Locate and identify every blood parasite.
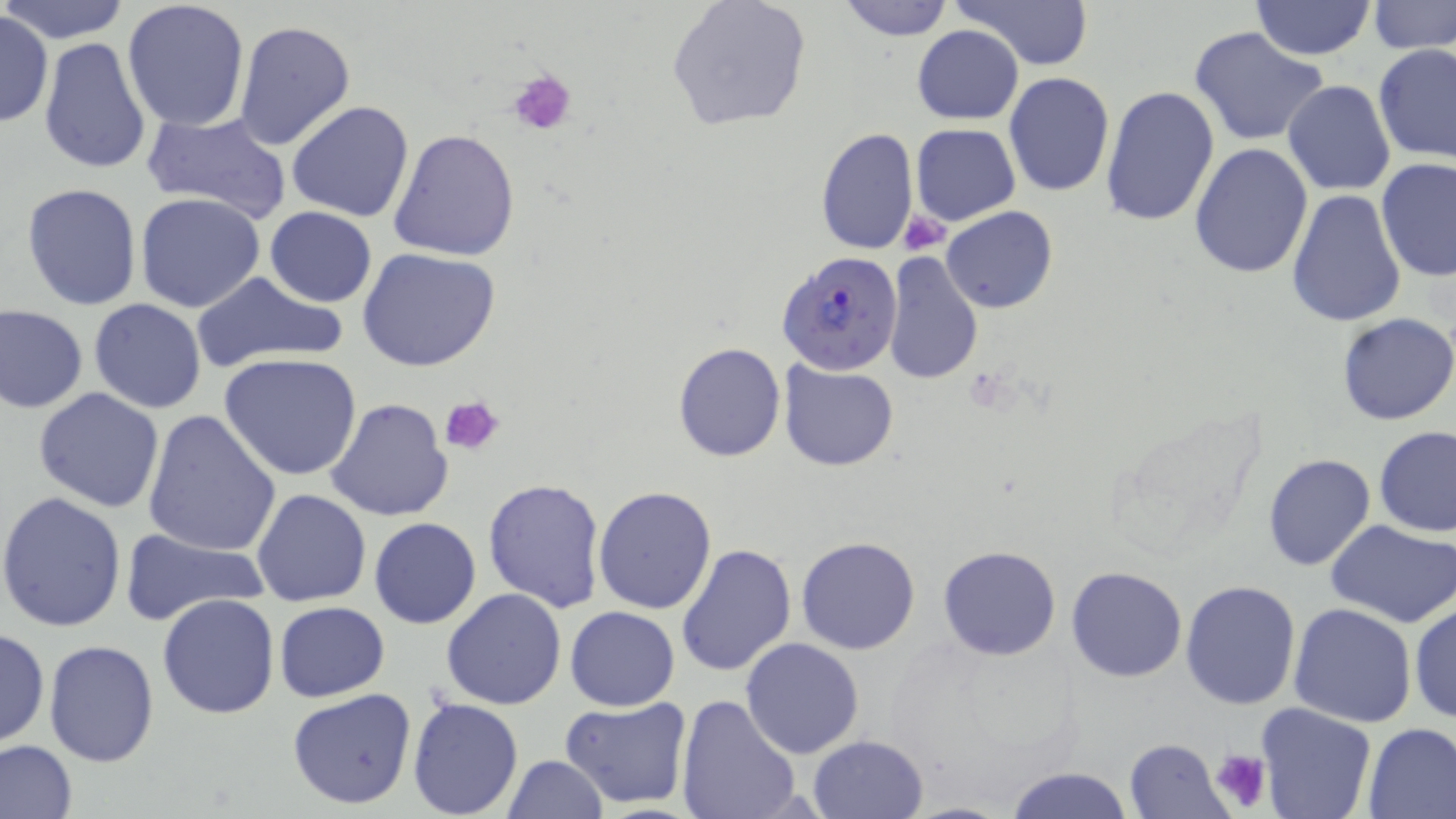

Approximate bounding boxes as [x1, y1, x2, y2] in pixels.
Plasmodium falciparum-infected red blood cells: [777, 248, 905, 376].
No Plasmodium ovale, Plasmodium malariae, Plasmodium vivax, Babesia divergens, or Trypanosoma brucei observed.

slide-level diagnosis = Plasmodium falciparum
image size = 1456×819 pixels
magnification = 1000x
stain = May-Grünwald-Giemsa
uninfected red blood cell locations = approximate bounding boxes as [x1, y1, x2, y2] in pixels: [0, 0, 131, 46], [835, 0, 956, 41], [953, 0, 1093, 71], [1251, 0, 1375, 60], [121, 1, 251, 133], [665, 1, 811, 131], [1368, 2, 1456, 54], [0, 12, 52, 128], [232, 20, 356, 152], [911, 25, 1025, 125], [1189, 26, 1330, 146], [38, 36, 154, 177], [1374, 45, 1456, 164], [1003, 72, 1115, 197], [1282, 80, 1396, 197], [1100, 86, 1220, 229], [286, 100, 416, 221], [141, 109, 293, 223], [910, 123, 1019, 226], [814, 126, 918, 257], [389, 128, 520, 261], [1188, 143, 1313, 280], [1374, 158, 1456, 283], [21, 183, 143, 312], [1285, 187, 1406, 330], [135, 192, 267, 313], [941, 205, 1057, 313], [266, 207, 377, 307], [356, 247, 502, 373], [883, 253, 984, 387], [192, 271, 347, 373], [88, 298, 206, 413], [1, 305, 88, 414], [1336, 312, 1456, 425], [673, 342, 786, 463], [219, 352, 366, 481], [779, 360, 899, 471], [33, 387, 165, 514], [325, 398, 455, 522], [140, 411, 282, 558], [1375, 426, 1456, 537], [1263, 453, 1376, 571], [482, 478, 606, 613], [592, 485, 718, 615], [251, 488, 373, 607], [0, 491, 128, 633], [369, 517, 480, 629], [1327, 520, 1456, 629], [118, 528, 269, 629], [795, 535, 920, 655], [676, 542, 799, 678], [937, 545, 1062, 661], [401, 554, 536, 705], [1064, 566, 1188, 682], [1179, 580, 1302, 709], [441, 589, 568, 710], [156, 593, 280, 720], [1409, 600, 1455, 725], [275, 601, 389, 701], [1289, 603, 1418, 728], [565, 606, 680, 711], [0, 628, 49, 748], [740, 636, 865, 759], [43, 639, 160, 768], [288, 688, 417, 810], [676, 694, 801, 819], [560, 696, 694, 808], [408, 697, 524, 818], [1255, 703, 1376, 819], [1361, 721, 1456, 819], [807, 734, 930, 819], [1125, 737, 1230, 819], [0, 739, 77, 819], [1015, 749, 1235, 817], [501, 756, 609, 818], [1005, 764, 1132, 819]
field of view = single
preparation = thin blood film
modality = light microscopy
platelet locations = approximate bounding boxes as [x1, y1, x2, y2] in pixels: [508, 69, 578, 138], [901, 211, 950, 253], [441, 394, 505, 455], [1211, 749, 1271, 813]